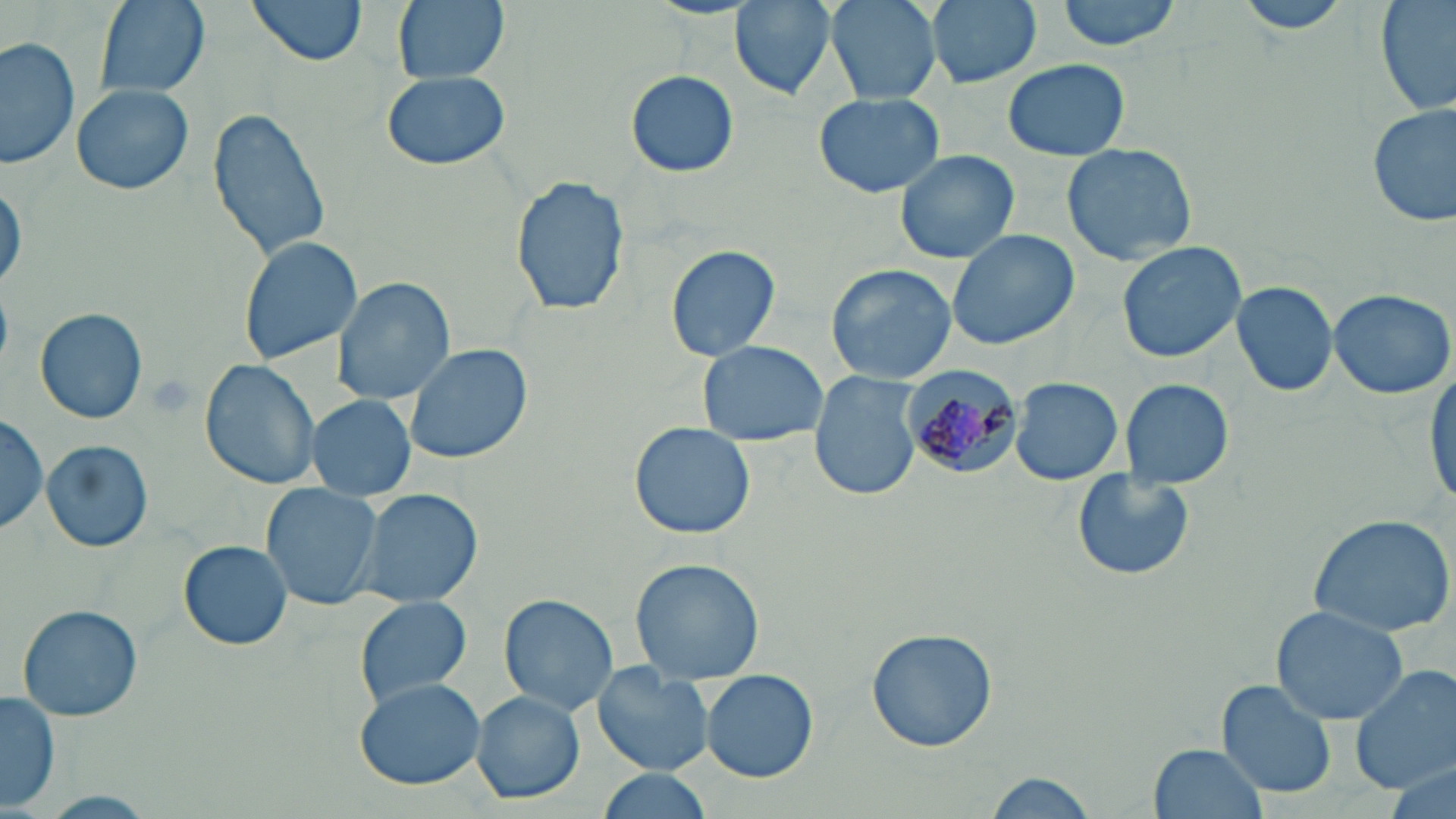
Approximate bounding boxes as (x1, y1, x2, y2) in pixels. Plasmodium malariae-infected red blood cell locations: (901, 367, 1024, 477). Uninfected red blood cell locations: (97, 0, 207, 97), (246, 0, 371, 65), (392, 0, 509, 84), (730, 0, 837, 99), (827, 0, 939, 104), (923, 0, 1044, 90), (1057, 0, 1180, 53), (1232, 0, 1358, 35), (1376, 0, 1455, 119), (0, 34, 79, 172), (1003, 58, 1129, 161), (379, 70, 512, 172), (626, 70, 739, 177), (72, 84, 193, 195), (813, 92, 944, 198), (1368, 103, 1454, 227), (207, 107, 332, 263), (1062, 141, 1199, 265), (894, 147, 1020, 265), (511, 174, 629, 319), (0, 178, 25, 295), (946, 227, 1079, 350), (237, 236, 363, 364), (1117, 241, 1245, 362), (665, 243, 781, 362), (825, 263, 957, 386), (333, 276, 455, 405), (1231, 281, 1338, 398), (1327, 287, 1455, 400), (35, 308, 150, 424), (698, 339, 827, 447), (402, 342, 532, 465), (200, 358, 324, 489), (1426, 367, 1456, 507), (810, 372, 923, 499), (1009, 377, 1124, 486), (1119, 379, 1234, 490), (308, 396, 414, 499), (0, 411, 47, 537), (629, 424, 755, 540), (42, 439, 153, 553), (1069, 469, 1196, 582), (261, 483, 384, 611), (355, 488, 483, 608), (1307, 512, 1456, 638), (179, 540, 293, 650), (629, 558, 766, 682), (500, 592, 619, 713), (356, 595, 472, 707), (16, 605, 143, 722), (1268, 606, 1409, 725), (866, 628, 1000, 753), (1350, 661, 1456, 795), (593, 667, 715, 775), (701, 669, 818, 783), (355, 679, 487, 790), (1213, 680, 1338, 799), (1, 688, 62, 813), (472, 690, 585, 804), (1150, 742, 1270, 819), (594, 770, 720, 819), (978, 771, 1098, 819). Slide-level diagnosis: Plasmodium malariae. May-Grünwald-Giemsa stain. One field of a larger specimen. Image is 1456×819 pixels. Thin blood film. Captured at 1000x magnification. Optical microscopy.